Comment on the background quality.
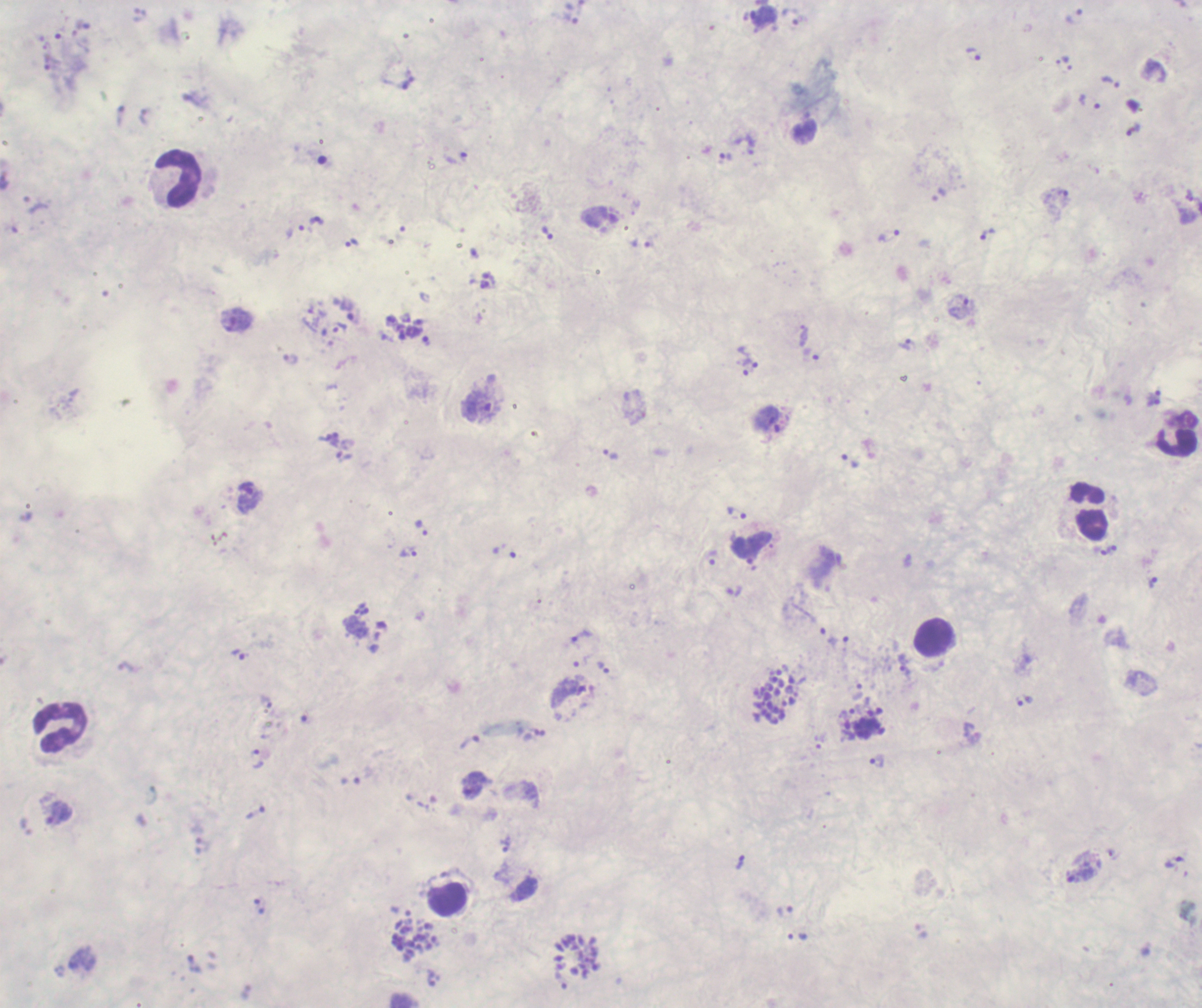
It is poor.

{
  "life_cycle_stages_observed": "trophozoite, schizont",
  "image_size": "1202×1008 pixels",
  "preparation": "thick blood film",
  "field_of_view": "one from this slide",
  "stain": "Romanowsky",
  "trophozoite_locations": "approximate object centers, in pixels from the top-left corner: (x=764, y=16), (x=793, y=17), (x=973, y=55), (x=1067, y=63), (x=1110, y=83), (x=1089, y=102), (x=725, y=158), (x=316, y=221), (x=548, y=234), (x=987, y=234), (x=890, y=237), (x=352, y=243), (x=959, y=307), (x=354, y=317), (x=233, y=319), (x=340, y=328), (x=804, y=335), (x=907, y=345), (x=749, y=358), (x=290, y=359), (x=482, y=406), (x=333, y=440), (x=610, y=454), (x=344, y=456), (x=249, y=497), (x=736, y=513), (x=421, y=528), (x=409, y=552), (x=712, y=557), (x=1153, y=583), (x=734, y=592), (x=582, y=637), (x=838, y=641), (x=238, y=654), (x=904, y=666), (x=604, y=668), (x=568, y=692), (x=1025, y=702), (x=257, y=759), (x=878, y=762), (x=472, y=786), (x=256, y=812), (x=59, y=814), (x=505, y=844), (x=1173, y=862), (x=1079, y=874), (x=785, y=912)",
  "leukocyte_locations": "approximate object centers, in pixels from the top-left corner: (x=179, y=179), (x=1178, y=434), (x=1090, y=513), (x=934, y=637), (x=61, y=728), (x=447, y=900)",
  "schizont_locations": "approximate object centers, in pixels from the top-left corner: (x=776, y=697), (x=865, y=722), (x=415, y=939), (x=576, y=956)",
  "context": "previously used in an actual diagnosis",
  "coloration_quality": "bad",
  "result": "malaria parasites detected",
  "magnification": "100x"
}